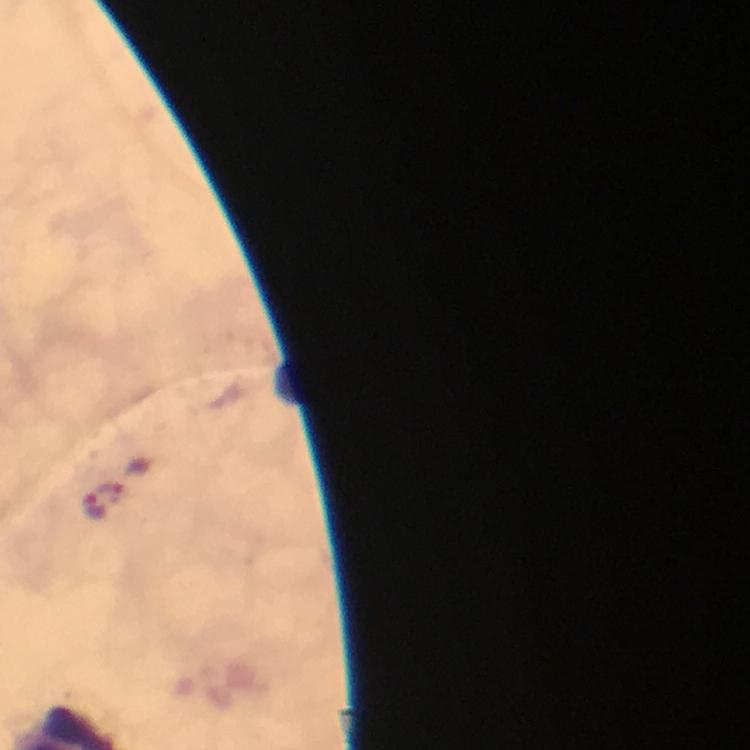

Approximate centers as {x, y} in pixels.
Summary:
  - Malaria parasite locations: {95, 506}
  - Cropped from: one field of view
  - Immersion oil: applied
  - Magnification: 100x
  - Preparation: thick smear
  - Image size: 750×750 pixels
  - Context: from a malaria diagnostic workup
  - Capture: smartphone photograph through a microscope
  - Stain: Giemsa